Locate every blood parasite and identify its species.
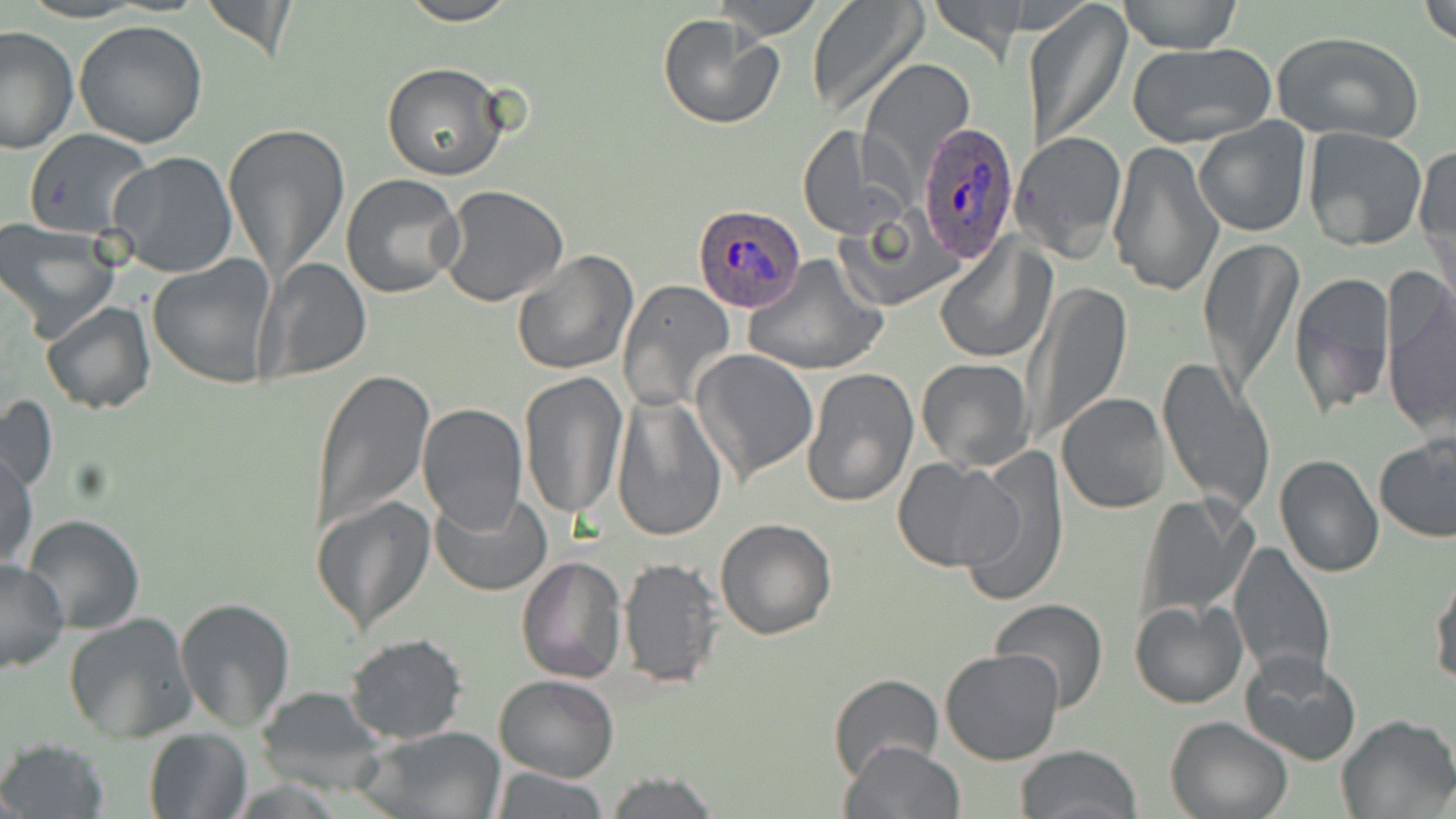
Approximate bounding boxes as named x1/y1/x2/y2 corners in pixels.
Plasmodium ovale-infected red blood cells: (x1=919, y1=122, x2=1021, y2=267), (x1=693, y1=202, x2=805, y2=311).
No Plasmodium falciparum, Plasmodium malariae, Plasmodium vivax, Babesia divergens, or Trypanosoma brucei observed.

slide-level diagnosis = Plasmodium ovale
uninfected red blood cell locations = approximate bounding boxes as named x1/y1/x2/y2 corners in pixels: (x1=201, y1=0, x2=298, y2=63), (x1=397, y1=0, x2=519, y2=25), (x1=713, y1=0, x2=824, y2=40), (x1=806, y1=0, x2=929, y2=119), (x1=930, y1=0, x2=1027, y2=64), (x1=1027, y1=0, x2=1132, y2=149), (x1=1117, y1=0, x2=1244, y2=53), (x1=1419, y1=0, x2=1455, y2=48), (x1=658, y1=12, x2=784, y2=129), (x1=74, y1=20, x2=209, y2=149), (x1=1, y1=25, x2=77, y2=155), (x1=1272, y1=29, x2=1425, y2=144), (x1=1125, y1=39, x2=1276, y2=149), (x1=860, y1=57, x2=973, y2=179), (x1=382, y1=63, x2=510, y2=183), (x1=1193, y1=116, x2=1311, y2=236), (x1=222, y1=120, x2=350, y2=286), (x1=798, y1=125, x2=905, y2=240), (x1=1302, y1=125, x2=1428, y2=250), (x1=24, y1=129, x2=153, y2=240), (x1=1023, y1=129, x2=1127, y2=258), (x1=1105, y1=138, x2=1226, y2=299), (x1=1415, y1=142, x2=1456, y2=282), (x1=108, y1=152, x2=239, y2=280), (x1=340, y1=173, x2=467, y2=299), (x1=438, y1=185, x2=569, y2=307), (x1=839, y1=210, x2=960, y2=312), (x1=1, y1=220, x2=119, y2=340), (x1=934, y1=233, x2=1051, y2=365), (x1=1198, y1=235, x2=1304, y2=395), (x1=510, y1=249, x2=638, y2=376), (x1=743, y1=255, x2=888, y2=377), (x1=148, y1=256, x2=279, y2=389), (x1=260, y1=258, x2=372, y2=382), (x1=1287, y1=268, x2=1398, y2=419), (x1=1381, y1=274, x2=1456, y2=435), (x1=618, y1=280, x2=737, y2=412), (x1=1025, y1=281, x2=1134, y2=446), (x1=40, y1=302, x2=156, y2=416), (x1=692, y1=349, x2=820, y2=483), (x1=1155, y1=356, x2=1277, y2=517), (x1=916, y1=358, x2=1034, y2=470), (x1=802, y1=366, x2=920, y2=508), (x1=310, y1=368, x2=435, y2=535), (x1=518, y1=372, x2=629, y2=523), (x1=1056, y1=392, x2=1173, y2=513), (x1=0, y1=394, x2=58, y2=496), (x1=611, y1=394, x2=729, y2=542), (x1=416, y1=402, x2=527, y2=534), (x1=1376, y1=433, x2=1455, y2=543), (x1=1, y1=450, x2=38, y2=573), (x1=955, y1=452, x2=1072, y2=604), (x1=1274, y1=454, x2=1384, y2=578), (x1=894, y1=457, x2=1018, y2=570), (x1=431, y1=490, x2=550, y2=596), (x1=1135, y1=492, x2=1257, y2=625), (x1=311, y1=494, x2=436, y2=637), (x1=20, y1=514, x2=146, y2=636), (x1=715, y1=519, x2=838, y2=639), (x1=1227, y1=543, x2=1336, y2=681), (x1=516, y1=554, x2=628, y2=683), (x1=618, y1=557, x2=722, y2=687), (x1=0, y1=558, x2=72, y2=675), (x1=1429, y1=565, x2=1456, y2=689), (x1=174, y1=598, x2=296, y2=731), (x1=990, y1=598, x2=1109, y2=714), (x1=1129, y1=599, x2=1248, y2=709), (x1=64, y1=612, x2=197, y2=743), (x1=344, y1=633, x2=468, y2=744), (x1=940, y1=647, x2=1067, y2=766), (x1=1239, y1=650, x2=1361, y2=766), (x1=827, y1=673, x2=944, y2=783), (x1=493, y1=674, x2=618, y2=782), (x1=254, y1=684, x2=389, y2=796), (x1=1335, y1=714, x2=1455, y2=819), (x1=1165, y1=716, x2=1293, y2=819), (x1=357, y1=726, x2=505, y2=819), (x1=143, y1=728, x2=252, y2=818), (x1=1, y1=738, x2=107, y2=818), (x1=838, y1=741, x2=967, y2=819), (x1=1015, y1=745, x2=1142, y2=819), (x1=489, y1=766, x2=611, y2=819), (x1=603, y1=769, x2=721, y2=818)
modality = light microscopy
image size = 1456×819 pixels
field of view = one of a larger specimen
stain = May-Grünwald-Giemsa
preparation = thin blood smear
magnification = 1000x